Locate and identify every blood parasite.
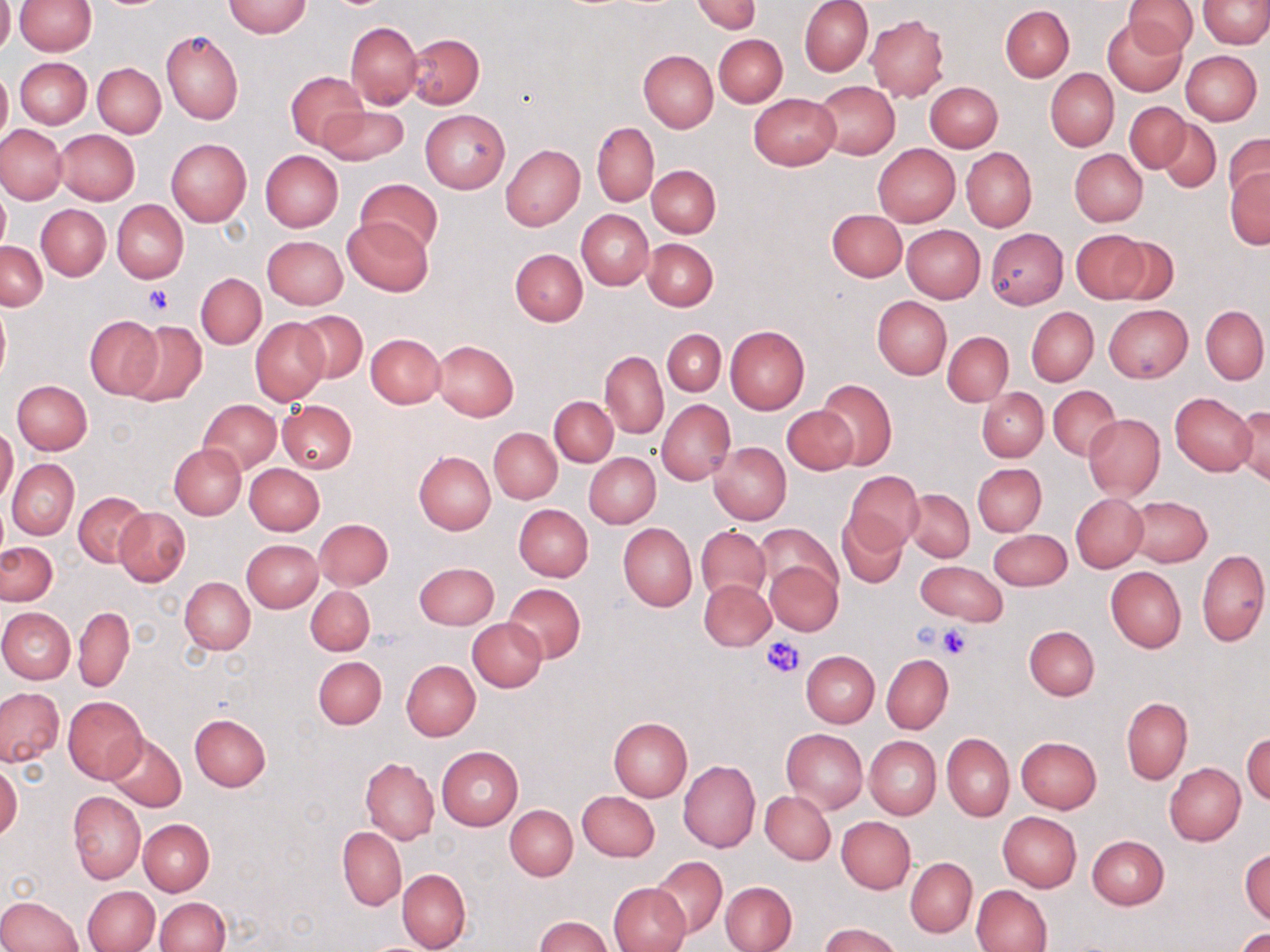

No blood parasites seen.

slide-level diagnosis = no evidence of blood parasites
stain = May-Grünwald-Giemsa
image size = 1270×952 pixels
magnification = 1000x
preparation = thin blood film
uninfected red blood cell locations = approximate bounding boxes as [x1, y1, x2, y2] in pixels: [0, 0, 14, 56], [14, 0, 96, 55], [693, 0, 760, 34], [799, 0, 873, 76], [1197, 0, 1270, 48], [224, 1, 311, 38], [1125, 1, 1197, 56], [1000, 5, 1074, 81], [866, 14, 950, 102], [1102, 16, 1189, 96], [346, 21, 422, 107], [162, 31, 243, 124], [405, 32, 484, 108], [714, 34, 787, 107], [638, 50, 717, 132], [1181, 50, 1261, 125], [15, 57, 91, 128], [93, 63, 166, 137], [0, 66, 11, 149], [1046, 69, 1119, 151], [286, 71, 366, 150], [813, 81, 899, 160], [926, 82, 1002, 152], [750, 93, 841, 169], [1125, 101, 1190, 173], [318, 105, 408, 164], [420, 110, 509, 193], [1155, 118, 1221, 192], [592, 122, 658, 207], [0, 124, 67, 204], [55, 129, 140, 205], [1223, 133, 1270, 205], [166, 139, 251, 226], [501, 144, 585, 230], [872, 144, 960, 227], [961, 149, 1035, 230], [1069, 149, 1146, 226], [260, 150, 343, 231], [647, 165, 720, 237], [1226, 168, 1270, 249], [356, 178, 443, 256], [0, 189, 9, 256], [113, 201, 188, 283], [37, 204, 110, 280], [827, 209, 907, 281], [577, 210, 652, 289], [342, 217, 433, 297], [902, 225, 985, 302], [985, 228, 1068, 309], [1072, 230, 1149, 302], [263, 235, 347, 310], [1109, 235, 1179, 307], [642, 238, 718, 310], [0, 241, 46, 310], [510, 248, 587, 325], [196, 272, 266, 349], [872, 296, 951, 380], [0, 303, 10, 384], [1103, 304, 1193, 383], [1201, 306, 1268, 383], [1026, 307, 1097, 385], [292, 310, 367, 383], [86, 315, 163, 400], [250, 318, 329, 404], [124, 320, 207, 407], [725, 325, 809, 413], [664, 328, 726, 396], [943, 332, 1013, 406], [366, 333, 446, 408], [431, 341, 519, 420], [601, 351, 668, 438], [815, 379, 897, 469], [12, 380, 92, 455], [1048, 386, 1120, 460], [978, 387, 1048, 461], [1170, 393, 1256, 475], [550, 397, 617, 466], [199, 399, 281, 474], [276, 400, 357, 474], [657, 400, 735, 485], [1230, 404, 1270, 484], [783, 407, 858, 475], [1083, 413, 1164, 499], [0, 424, 18, 504], [489, 428, 562, 503], [709, 441, 791, 525], [170, 443, 246, 519], [414, 450, 496, 535], [585, 453, 661, 527], [8, 459, 78, 539], [243, 463, 325, 536], [973, 463, 1046, 536], [844, 471, 924, 554], [904, 489, 973, 562], [75, 492, 150, 567], [1070, 494, 1147, 572], [1126, 496, 1211, 566], [513, 504, 592, 581], [114, 507, 190, 586], [836, 511, 906, 588], [315, 518, 393, 589], [618, 523, 697, 611], [756, 524, 840, 597], [696, 526, 771, 604], [988, 529, 1071, 591], [242, 539, 322, 613], [1, 541, 56, 606], [1196, 549, 1269, 648], [765, 561, 842, 636], [916, 561, 1008, 625], [413, 562, 499, 629], [1106, 565, 1186, 653], [180, 577, 255, 654], [699, 579, 775, 651], [502, 582, 585, 663], [306, 586, 375, 656], [74, 606, 134, 693], [0, 607, 75, 684], [468, 618, 547, 692], [1024, 625, 1099, 700], [801, 651, 879, 727], [881, 655, 953, 733], [313, 656, 386, 729], [401, 660, 480, 741], [0, 688, 65, 767], [64, 696, 147, 782], [1122, 697, 1192, 784], [189, 713, 271, 791], [609, 717, 693, 801], [781, 728, 867, 814], [1244, 730, 1270, 804], [104, 732, 186, 812], [942, 734, 1015, 821], [865, 736, 940, 819], [1016, 736, 1101, 812], [437, 747, 523, 830], [361, 758, 439, 843], [678, 759, 760, 852], [0, 761, 21, 843], [1164, 763, 1245, 845], [578, 790, 659, 860], [68, 791, 146, 883], [760, 791, 835, 865], [505, 805, 577, 880], [997, 811, 1081, 891], [837, 816, 916, 893], [140, 819, 215, 895], [337, 828, 406, 910], [1087, 834, 1169, 910], [1241, 849, 1270, 925], [652, 855, 727, 938], [905, 857, 977, 937], [398, 869, 471, 952], [608, 881, 691, 952], [721, 881, 796, 952], [971, 884, 1052, 951], [83, 885, 159, 952], [0, 894, 83, 951], [155, 897, 230, 952], [534, 916, 612, 952], [820, 923, 900, 952], [1236, 928, 1270, 951]
platelet locations = approximate bounding boxes as [x1, y1, x2, y2] in pixels: [144, 283, 172, 315], [911, 620, 954, 654], [934, 623, 974, 660], [763, 636, 806, 680]
field of view = one of a larger specimen
modality = optical microscopy